Comment on the morphology of the erythrocytes.
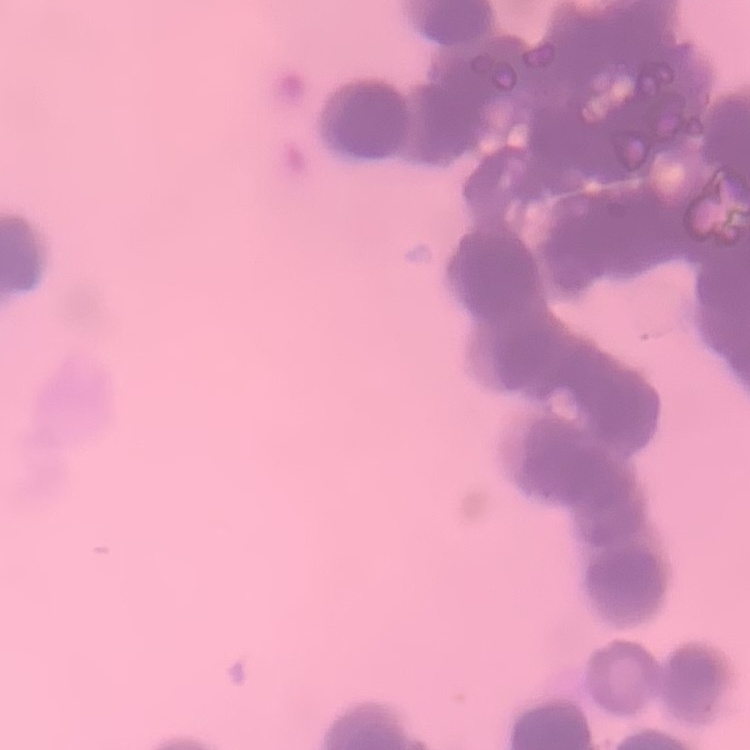
They show rouleaux formation.

Stained with either Field's or Giemsa. Thin blood smear. One tile cut from a larger photomicrograph.